Give the extent of all Plasmodium falciparum-infected red blood cells.
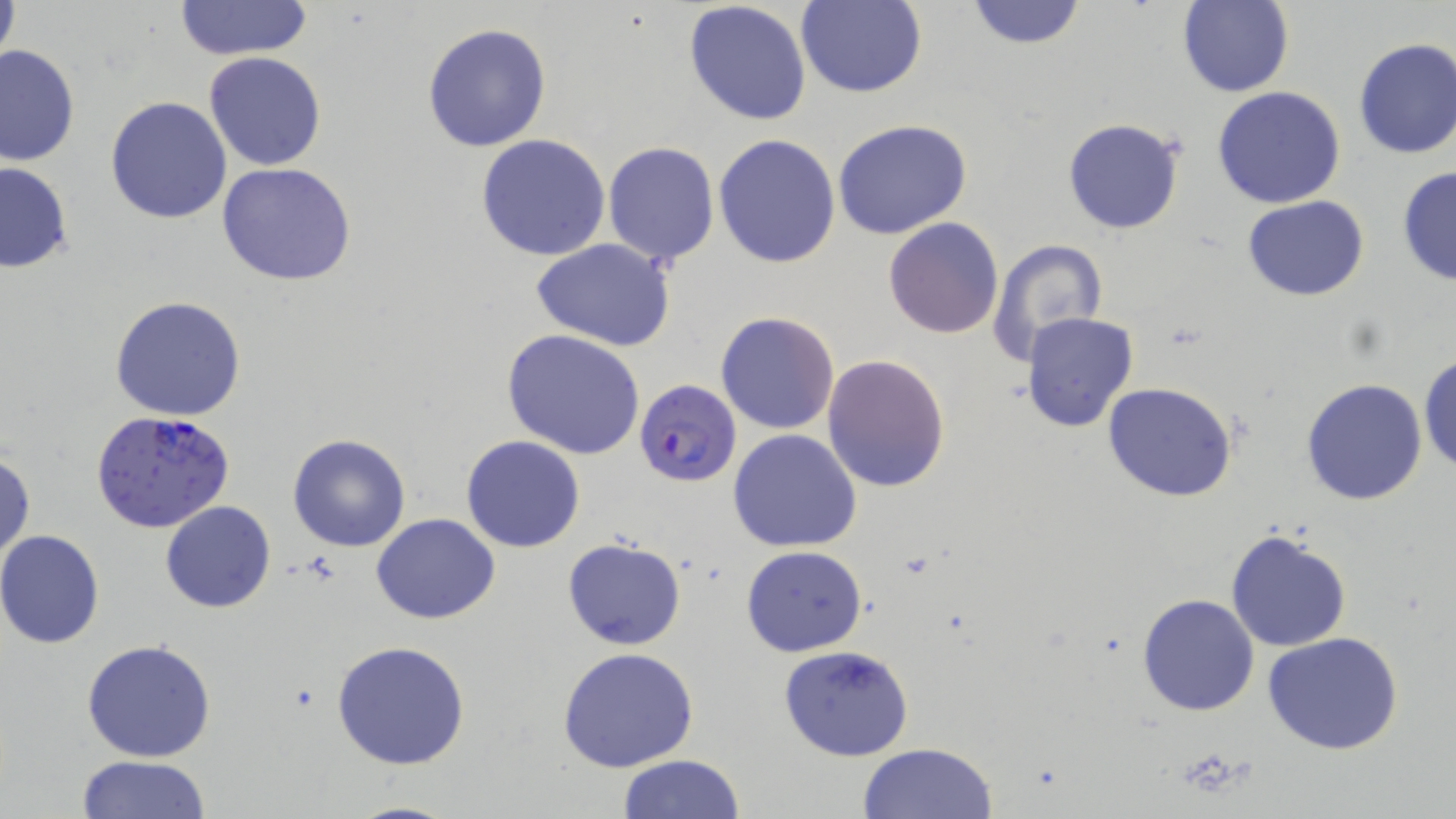
Approximate bounding boxes as [x1, y1, x2, y2] in pixels.
Plasmodium falciparum-infected red blood cells: [638, 381, 745, 487], [89, 411, 236, 534].

Uninfected red blood cell locations: [0, 0, 21, 78], [796, 0, 927, 98], [963, 0, 1088, 51], [174, 1, 315, 62], [684, 1, 813, 127], [1176, 1, 1293, 98], [422, 22, 552, 153], [1352, 37, 1456, 160], [0, 43, 80, 167], [204, 52, 326, 170], [1212, 85, 1346, 209], [105, 95, 233, 224], [1062, 118, 1185, 235], [832, 121, 974, 240], [713, 133, 840, 268], [476, 134, 612, 261], [603, 141, 720, 267], [0, 161, 73, 274], [217, 162, 357, 286], [1396, 165, 1456, 287], [1242, 196, 1369, 301], [883, 217, 1003, 338], [986, 238, 1108, 366], [531, 239, 675, 351], [111, 296, 246, 421], [715, 311, 840, 434], [1023, 312, 1140, 433], [502, 330, 645, 461], [822, 353, 951, 492], [1419, 354, 1456, 475], [1300, 378, 1429, 504], [1102, 382, 1240, 502], [727, 429, 862, 552], [287, 432, 413, 552], [461, 435, 584, 552], [0, 450, 35, 566], [160, 502, 275, 613], [371, 514, 500, 624], [1226, 530, 1351, 651], [0, 531, 104, 648], [561, 535, 688, 650], [740, 545, 869, 658], [1135, 593, 1258, 717], [1263, 633, 1406, 755], [80, 638, 217, 762], [331, 639, 475, 772], [778, 644, 914, 761], [556, 646, 700, 772], [859, 744, 999, 819], [617, 754, 747, 818], [75, 755, 211, 819], [343, 799, 466, 819]. Slide-level diagnosis: Plasmodium falciparum. 1000x magnification. Optical microscopy. Image is 1456×819 pixels. Single field of view. May-Grünwald-Giemsa stain. Thin blood smear.